State which parasite is depicted.
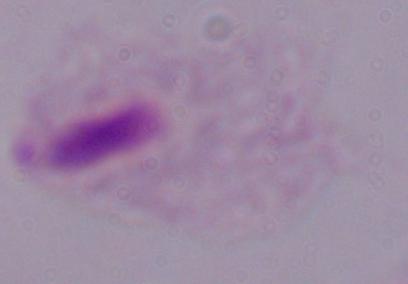
This is a trichomonad.

Summary:
  - Modality: photomicrograph
  - Magnification: 1000x